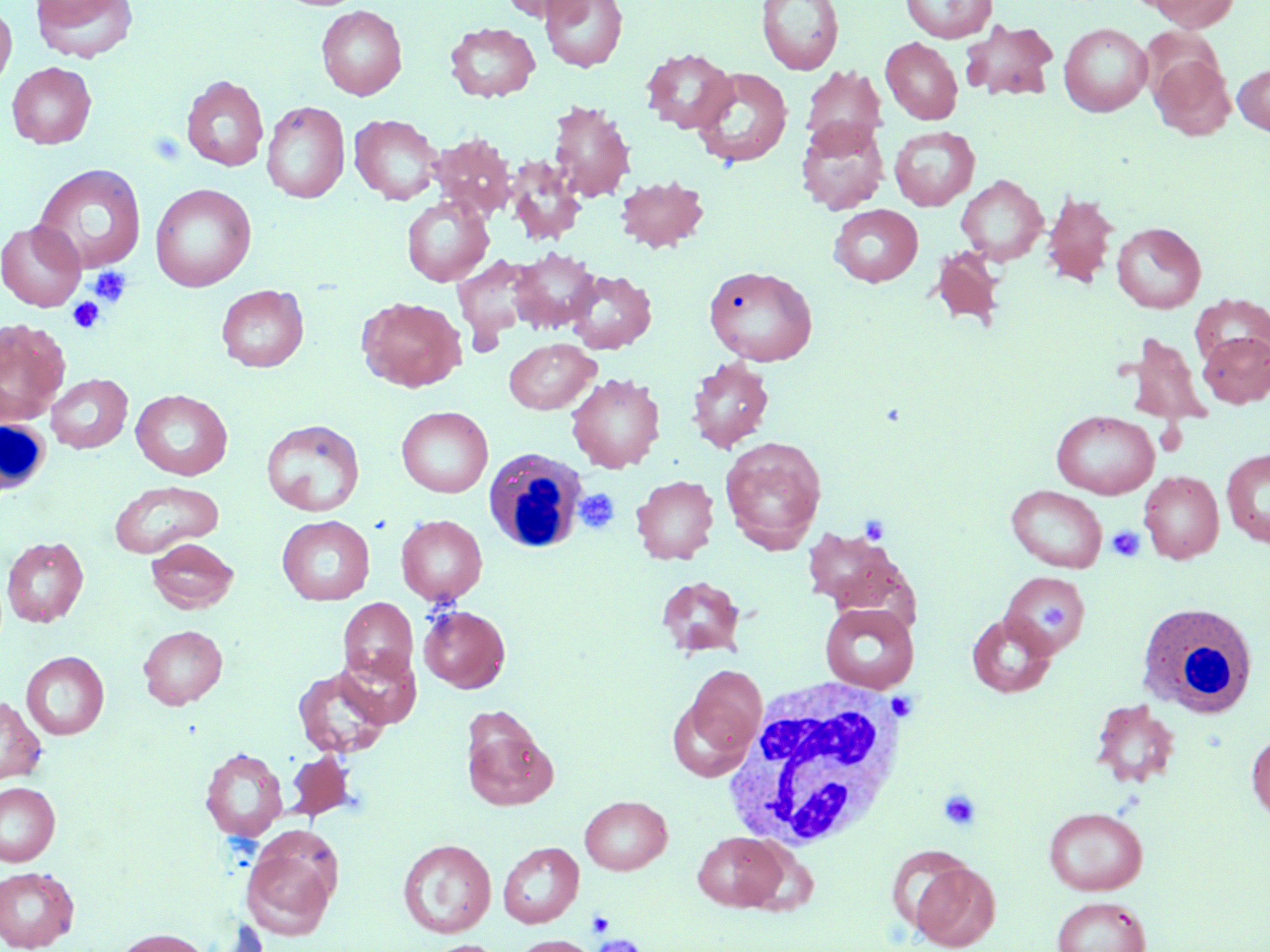
Summary:
  - Coordinate format: approximate bounding boxes as (x1, y1, x2, y2) in pixels
  - Platelet locations: (149, 131, 186, 166), (88, 266, 132, 308), (67, 297, 105, 333), (575, 489, 620, 533), (859, 515, 890, 545), (1107, 525, 1145, 562), (1041, 602, 1069, 632), (886, 691, 918, 722), (938, 789, 983, 832), (587, 910, 615, 936), (591, 934, 648, 952)
  - Uninfected red blood cell locations: (30, 0, 138, 63), (501, 0, 592, 22), (540, 0, 627, 71), (756, 0, 844, 75), (900, 0, 996, 42), (1141, 0, 1240, 31), (0, 3, 16, 93), (316, 5, 407, 101), (961, 19, 1058, 102), (445, 22, 540, 102), (1059, 23, 1152, 116), (1139, 26, 1224, 100), (881, 37, 963, 124), (642, 48, 737, 133), (1149, 53, 1235, 141), (7, 62, 97, 149), (1233, 63, 1270, 135), (800, 65, 887, 151), (691, 67, 794, 168), (181, 75, 268, 171), (547, 100, 636, 203), (261, 101, 350, 203), (350, 115, 443, 204), (796, 119, 889, 214), (889, 127, 979, 210), (527, 129, 623, 231), (429, 133, 516, 218), (505, 157, 585, 245), (32, 164, 147, 274), (615, 175, 709, 253), (956, 175, 1048, 265), (150, 183, 256, 292), (1041, 190, 1119, 287), (401, 196, 494, 286), (829, 204, 923, 286), (0, 220, 86, 311), (1111, 222, 1206, 313), (928, 245, 1008, 329), (509, 247, 602, 334), (453, 255, 539, 342), (704, 264, 817, 366), (566, 268, 656, 353), (216, 284, 309, 372), (1191, 295, 1270, 368), (357, 296, 466, 392), (0, 319, 70, 424), (1197, 331, 1270, 408), (1124, 333, 1211, 425), (504, 339, 599, 414), (686, 357, 774, 453), (566, 372, 665, 473), (46, 373, 132, 453), (131, 389, 233, 480), (396, 406, 493, 497), (1052, 410, 1159, 499), (261, 419, 365, 517), (720, 437, 826, 552), (1220, 449, 1270, 548), (1139, 471, 1224, 563), (631, 475, 719, 564), (108, 480, 224, 558), (1006, 485, 1108, 573), (396, 514, 487, 605), (277, 515, 375, 605), (803, 528, 903, 611), (2, 536, 88, 627), (146, 537, 239, 613), (1000, 570, 1090, 657), (656, 576, 746, 659), (338, 597, 417, 684), (820, 602, 919, 693), (419, 605, 510, 692), (967, 613, 1057, 698), (138, 624, 227, 709), (335, 648, 422, 728), (21, 651, 109, 740), (684, 664, 766, 760), (293, 668, 390, 758), (0, 696, 47, 785), (1090, 699, 1180, 789), (461, 709, 556, 811), (1246, 729, 1270, 824), (200, 747, 288, 841), (285, 751, 356, 822), (0, 781, 60, 866), (580, 795, 672, 874), (1044, 807, 1147, 895), (692, 831, 789, 912), (397, 838, 496, 938), (498, 842, 584, 928), (240, 843, 337, 939), (883, 844, 977, 936), (909, 860, 1001, 951), (0, 866, 79, 951), (1052, 896, 1152, 952), (112, 928, 212, 952), (510, 935, 597, 952), (425, 940, 505, 952)
  - White blood cell locations: (0, 415, 51, 500), (484, 448, 587, 554), (1136, 601, 1259, 719), (722, 679, 912, 852)
  - Slide-level diagnosis: negative for blood parasites
  - Stain: May-Grünwald-Giemsa
  - Image size: 1270×952 pixels
  - Preparation: thin blood smear
  - Magnification: 1000x
  - Modality: optical microscopy
  - Field of view: single